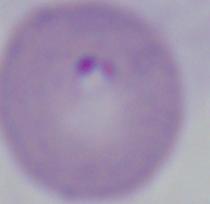
Summary:
  - Identification: Babesia
  - Modality: micrograph
  - Magnification: 1000x